Comment on the morphology of the red blood cells.
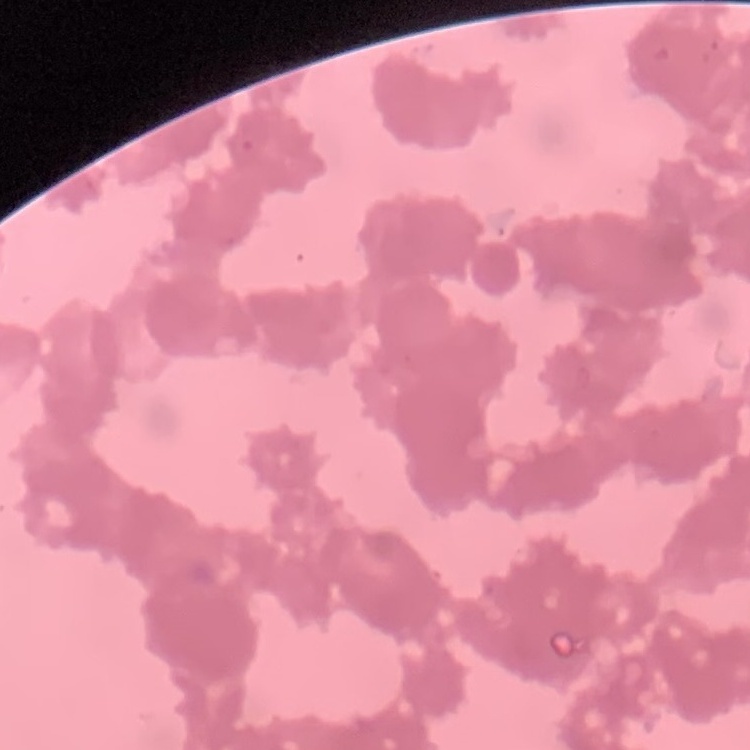

Rouleaux formation.

image type = one tile cut from a larger photomicrograph
preparation = thin blood film
stain = Field's or Giemsa